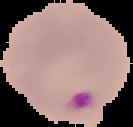
Image is 133×127 pixels. From a thin blood smear. Result: malaria parasites detected. Cell region segmented out of the field of view; the surrounding area is masked to black.